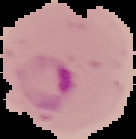
Summary:
  - Image size: 136×139 pixels
  - Result: Plasmodium parasites identified
  - Image type: cell region segmented out of the field of view; surrounding area masked to black
  - Preparation: thin blood smear